Report the malaria status of this cell.
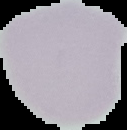
Uninfected.

image type = cell region segmented out of the field of view; surrounding area masked to black
image size = 127×130 pixels
preparation = thin blood film